Classify this cell by malaria status.
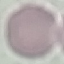
It is uninfected.

Cell patch, automatically extracted from a larger field of view and resized to 64 × 64 pixels. Giemsa stain. Photographed with a smartphone camera at the microscope eyepiece. Thin blood smear.